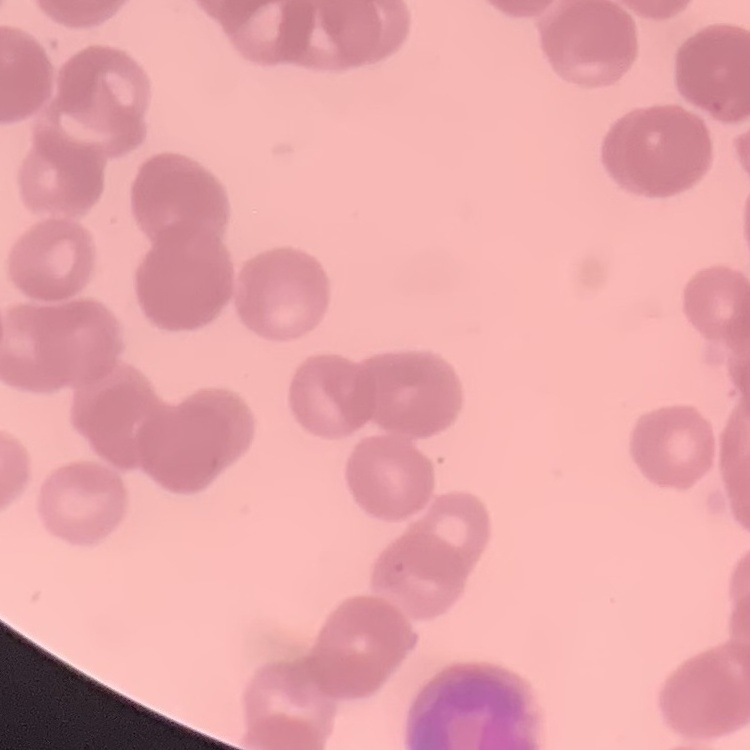
red blood cell morphology = rouleaux formation
image type = square crop of a larger photomicrograph
stain = Field's or Giemsa
preparation = thin peripheral smear